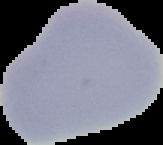

{
  "image_size": "163×145 pixels",
  "result": "negative for Plasmodium parasites",
  "preparation": "thin blood film",
  "image_type": "cell region segmented out of the field of view; surrounding area masked to black"
}